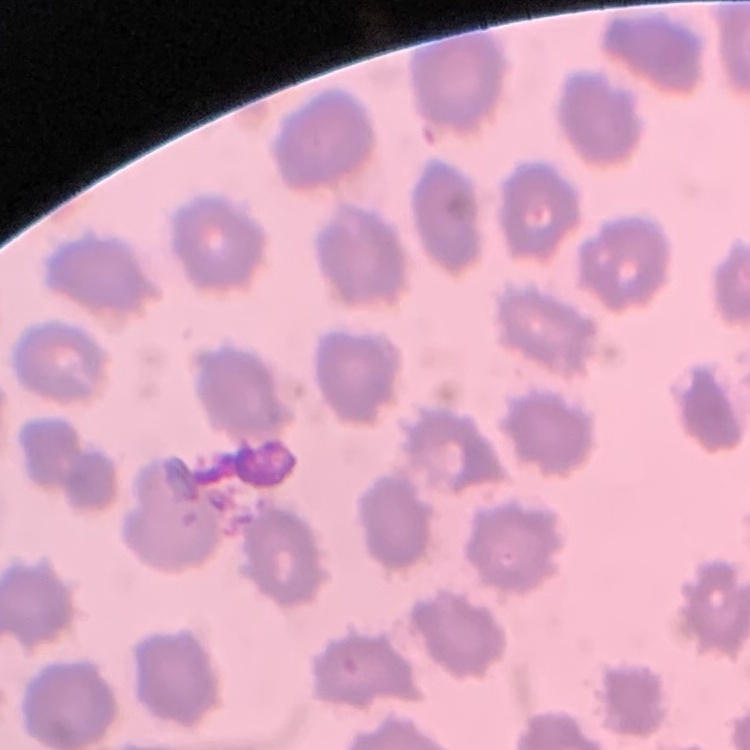
red blood cell morphology = no rouleaux formation
image type = square crop of a larger photomicrograph
stain = Field's or Giemsa
preparation = thin blood film